Give the position of every malaria parasite.
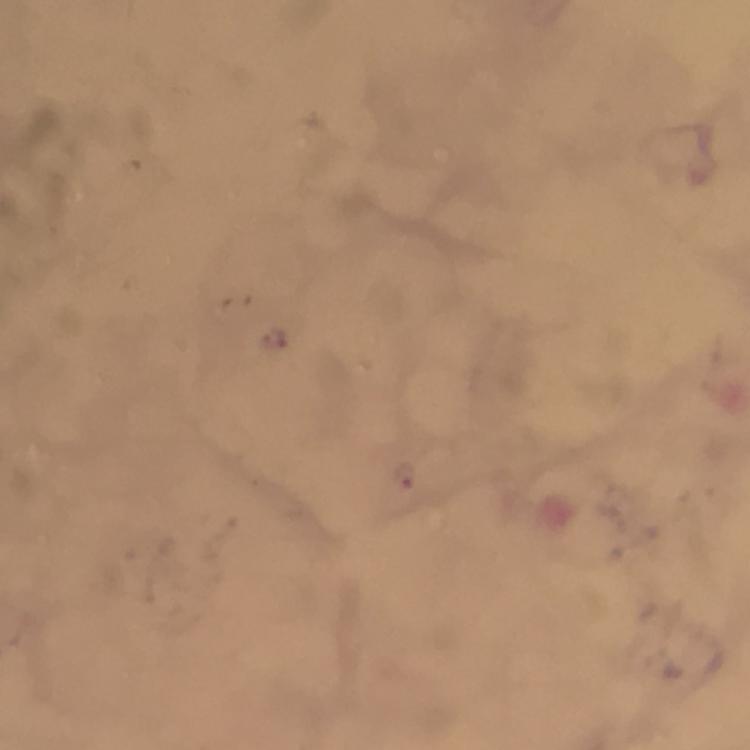
Approximate centers as [x, y] in pixels.
Malaria parasites: [271, 336], [405, 473].

cropped from = one field of view
stain = Giemsa
capture = smartphone camera through the microscope
immersion oil = applied
image size = 750×750 pixels
magnification = 100x
context = from a diagnostic examination for malaria
preparation = thick blood film